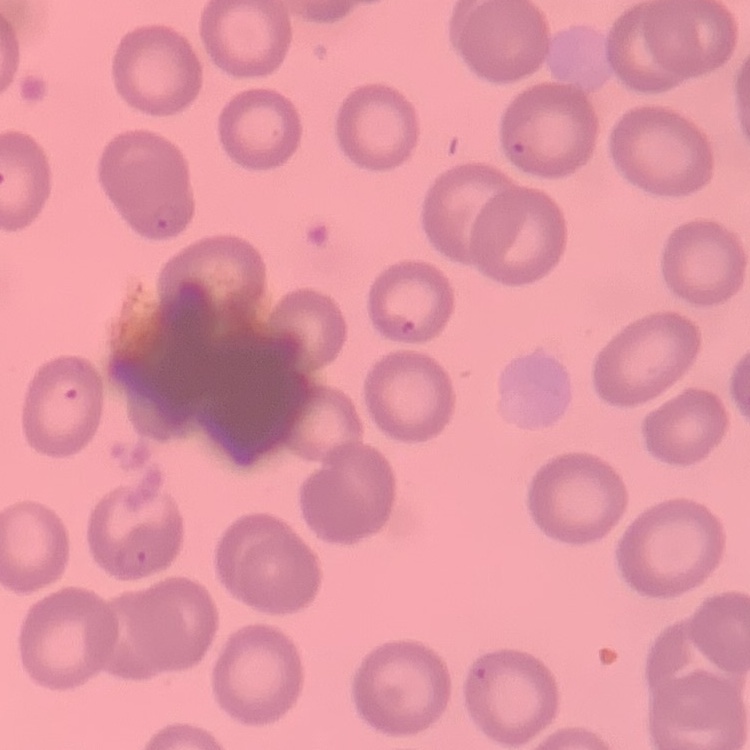
Summary:
  - Erythrocyte morphology: no rouleaux formation
  - Stain: Field's or Giemsa
  - Preparation: thin blood film
  - Image type: one tile cut from a larger photomicrograph